Assess for Plasmodium parasites.
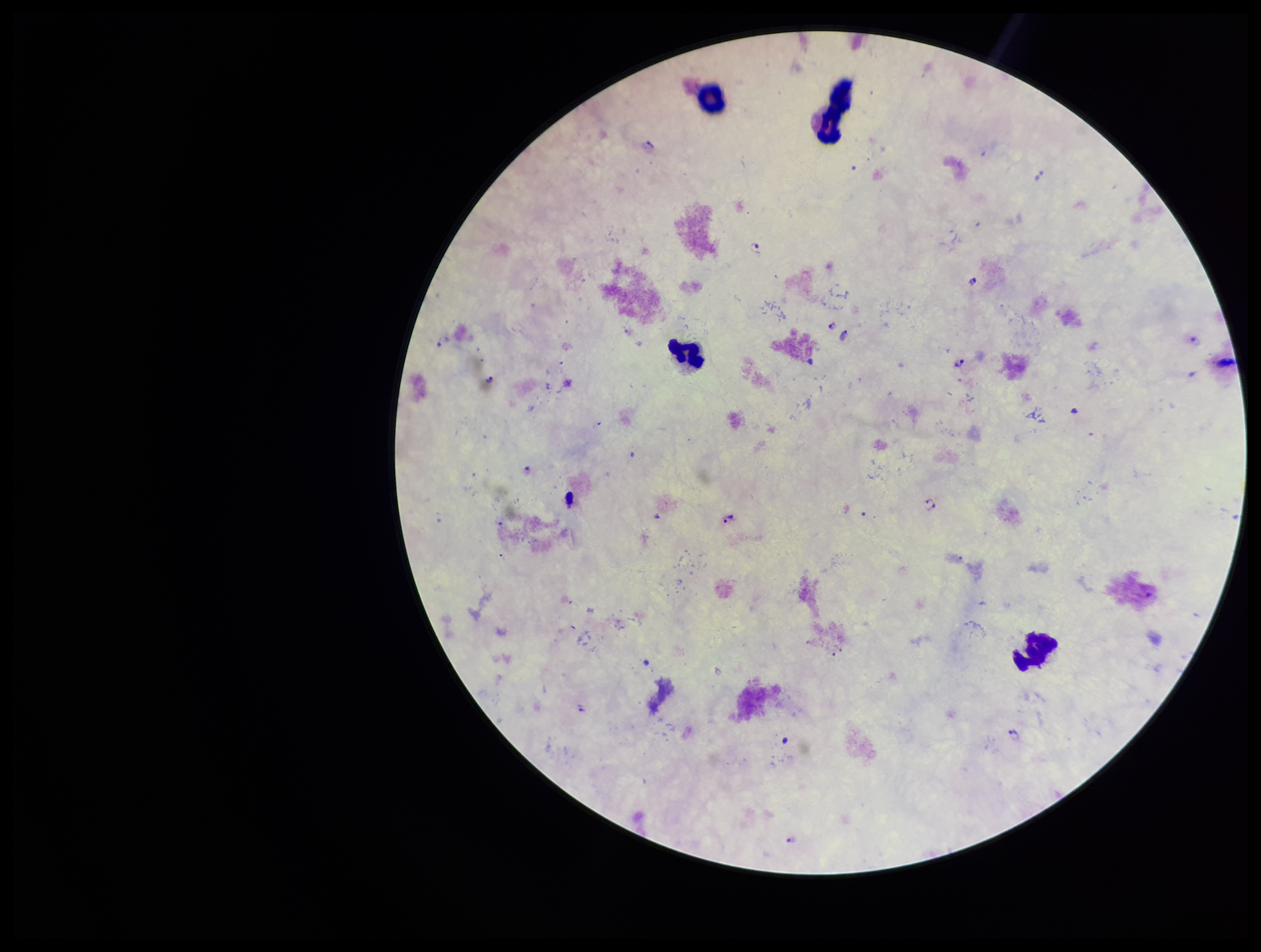

Detected.

Giemsa stain. Smartphone photograph taken through the eyepiece of a microscope. Preparation: thick. Single field of view. Patient malaria status: infected. Parasite count: 9. Image is 1261×952 pixels. Leukocyte count: 4. Species reported for this patient: Plasmodium falciparum.